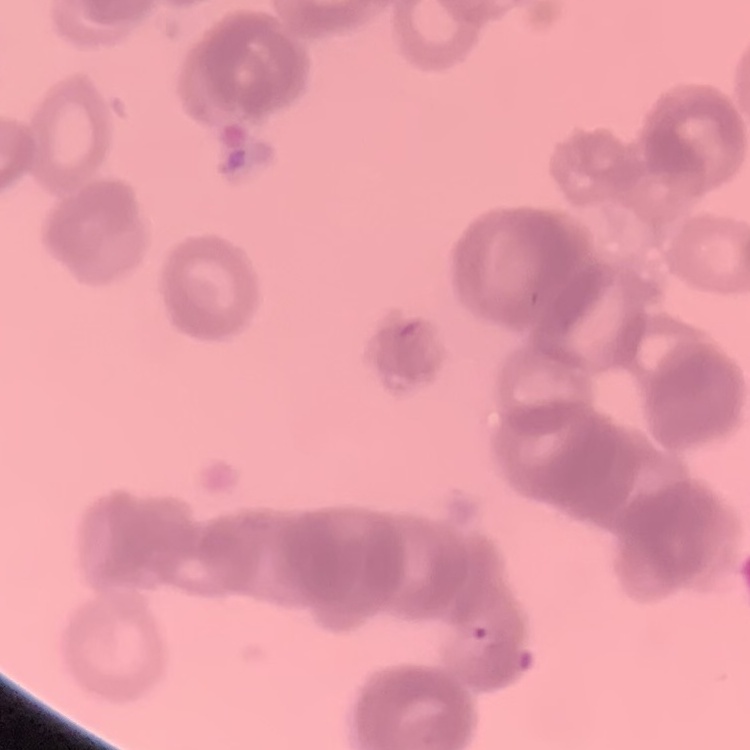

The red blood cells show rouleaux formation. Square crop of a larger photomicrograph. Thin blood smear. Field's or Giemsa stain.